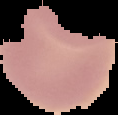
Image is 118×115 pixels. From a thin blood smear. Malaria status: uninfected. Segmented cell region on a black background.